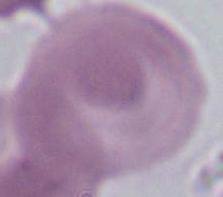
Photomicrograph. A red blood cell is shown. Captured at 1000x magnification.